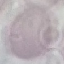
Summary:
  - Malaria status: uninfected
  - Capture: smartphone through the microscope eyepiece
  - Image type: cell patch, automatically extracted from a larger field of view and resized to 64 × 64 pixels
  - Preparation: thin blood film
  - Stain: Giemsa